Assess this cell for malaria.
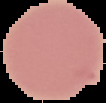
It is uninfected.

image size = 106×103 pixels
image type = segmented cell region on a black background
preparation = thin blood smear